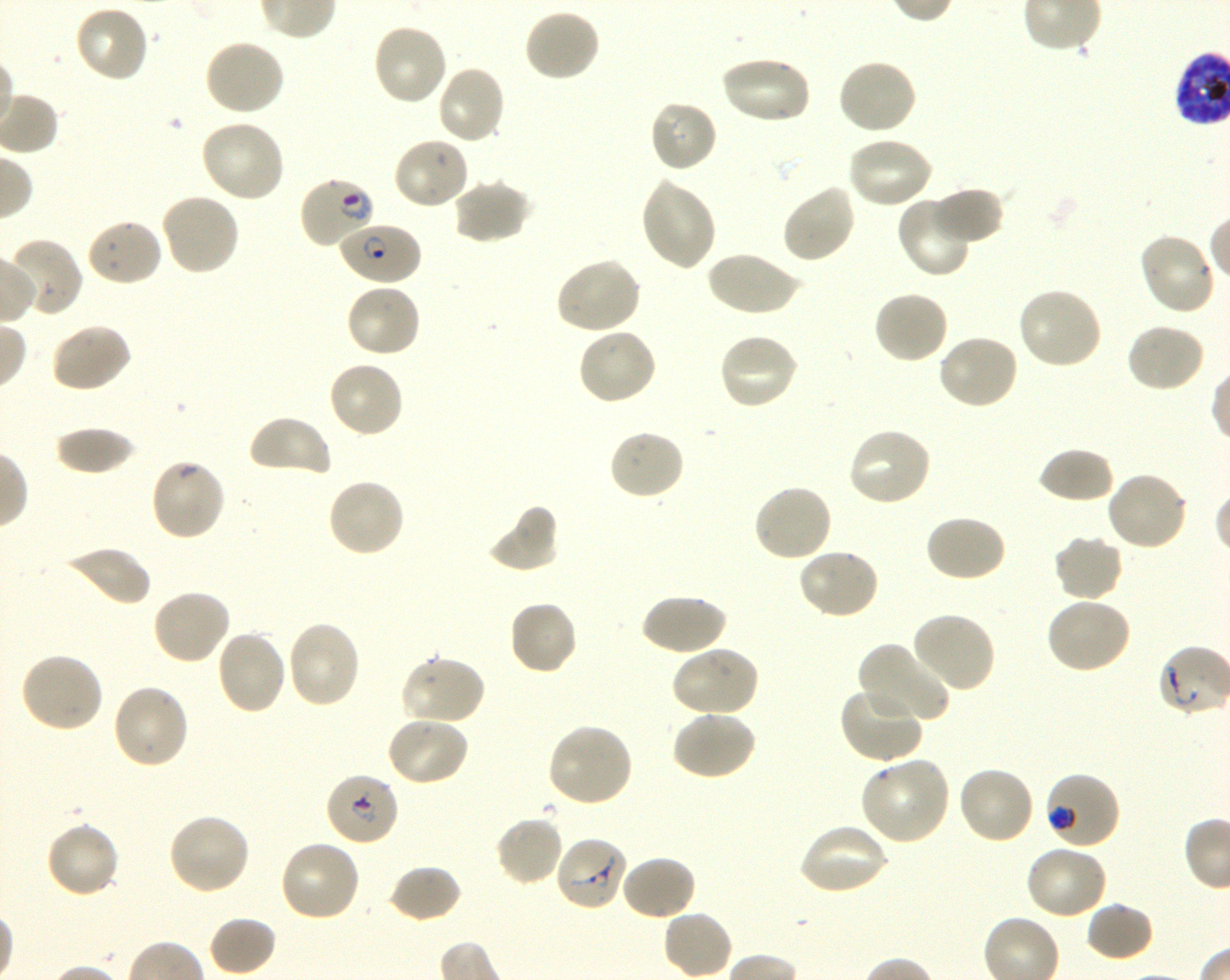
Not every red blood cell is marked. A life-cycle stage — or a range of stages, where the recorded stages span more than one — follows each staged infected red blood cell.
{
  "locations_of_uninfected_red_blood_cells": "approximate bounding boxes as (x1, y1, x2, y2) in pixels: (74, 5, 151, 83), (523, 7, 602, 82), (371, 22, 448, 106), (204, 38, 286, 117), (719, 55, 812, 126), (835, 59, 918, 136), (435, 63, 506, 145), (647, 98, 719, 173), (201, 118, 286, 203), (846, 134, 934, 209), (392, 136, 472, 211), (639, 176, 718, 272), (452, 178, 531, 245), (780, 182, 857, 264), (930, 186, 1005, 246), (159, 192, 240, 277), (896, 194, 974, 278), (85, 217, 164, 287), (1138, 232, 1215, 315), (6, 238, 83, 317), (706, 249, 803, 317), (555, 257, 643, 336), (345, 282, 422, 358), (1016, 286, 1105, 371), (872, 290, 949, 365), (50, 322, 133, 394), (1125, 323, 1206, 393), (577, 327, 658, 406), (717, 332, 800, 412), (936, 333, 1020, 412), (327, 360, 406, 439), (247, 414, 332, 479), (53, 426, 139, 476), (846, 426, 932, 507), (607, 428, 687, 501), (1036, 446, 1115, 504), (1105, 471, 1189, 552), (326, 477, 406, 558), (752, 483, 833, 563), (484, 503, 560, 573), (922, 514, 1007, 583), (1052, 534, 1125, 603), (61, 545, 151, 608), (797, 547, 881, 621), (152, 588, 232, 666), (640, 592, 727, 657), (1045, 596, 1132, 674), (507, 599, 579, 676), (910, 611, 998, 693), (286, 620, 362, 710), (214, 629, 287, 715), (857, 640, 952, 725), (670, 645, 760, 718), (18, 651, 105, 733), (400, 654, 486, 727), (112, 683, 191, 770), (838, 684, 923, 764), (671, 710, 757, 781), (386, 714, 469, 786), (546, 722, 635, 808), (857, 755, 952, 845), (955, 765, 1035, 846), (167, 812, 252, 896), (493, 814, 564, 886), (45, 820, 122, 899), (797, 821, 889, 896), (278, 839, 362, 924), (1024, 844, 1109, 921), (620, 853, 697, 922), (388, 864, 463, 924), (1084, 901, 1155, 962), (207, 915, 277, 977)",
  "life_cycle_stages_observed": "ring, trophozoite",
  "donor_blood_group": "O+",
  "field_of_view": "single",
  "objective": "100x, oil immersion, numerical aperture 1.30",
  "locations_of_infected_red_blood_cells": "approximate bounding boxes as (x1, y1, x2, y2) in pixels: (298, 175, 377, 250) early ring to early trophozoite; (337, 221, 422, 286) ring; (324, 770, 400, 846) ring; (1044, 770, 1122, 849) early trophozoite",
  "image_size": "1230×980 pixels",
  "stain": "Giemsa",
  "preparation": "thin blood smear",
  "locations_of_red_blood_cells_of_indeterminate_infection_status": "approximate bounding boxes as (x1, y1, x2, y2) in pixels: (149, 457, 227, 542), (554, 836, 629, 912)",
  "culture": "shaking in-vitro P. falciparum strain 3D7"
}